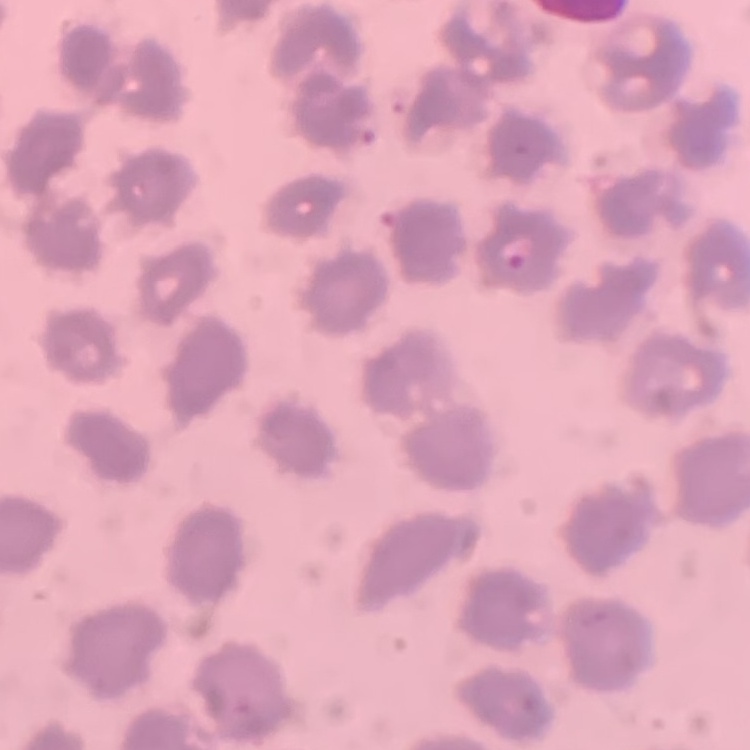

Summary:
  - Erythrocyte morphology: no rouleaux formation
  - Stain: Field's or Giemsa
  - Image type: square crop of a larger photomicrograph
  - Preparation: thin blood film